Identify the parasite.
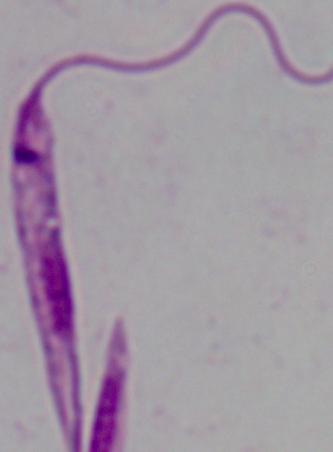

Leishmania.

modality: photomicrograph
magnification: 1000x